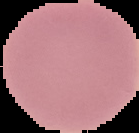 From a thin blood film. Result: negative for Plasmodium parasites. Image is 139×133 pixels. The area outside the segmented cell region is set to black.